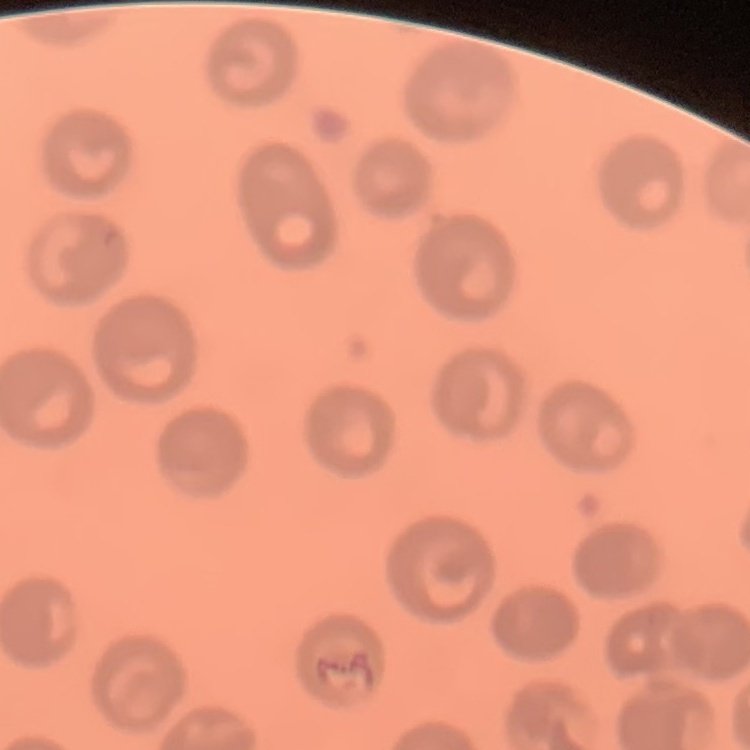
Summary:
  - Red blood cell morphology: no rouleaux formation
  - Stain: Field's or Giemsa
  - Preparation: thin blood film
  - Image type: one tile cut from a larger photomicrograph